Assess this cell for malaria.
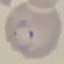
Parasitized.

Giemsa stain. Thin blood smear. Acquired by smartphone through the microscope eyepiece. Cell patch, automatically extracted from a larger field of view and resized to 64 × 64 pixels.